State which parasite is depicted.
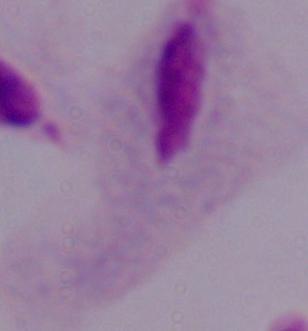
This is a trichomonad.

modality = photomicrograph
magnification = 1000x